Comment on the morphology of the erythrocytes.
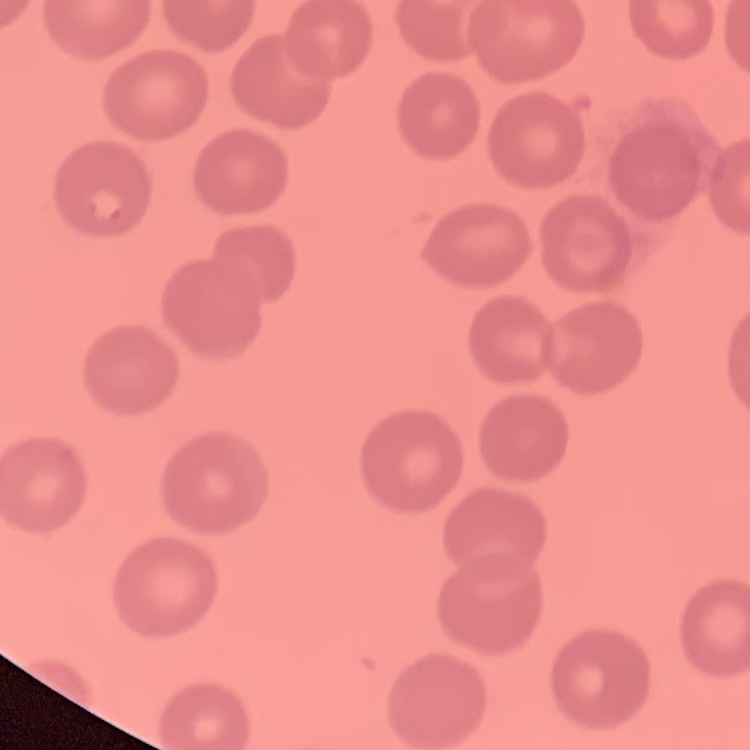

They show no rouleaux formation.

image_type: square crop of a larger photomicrograph
preparation: thin blood film
stain: Field's or Giemsa